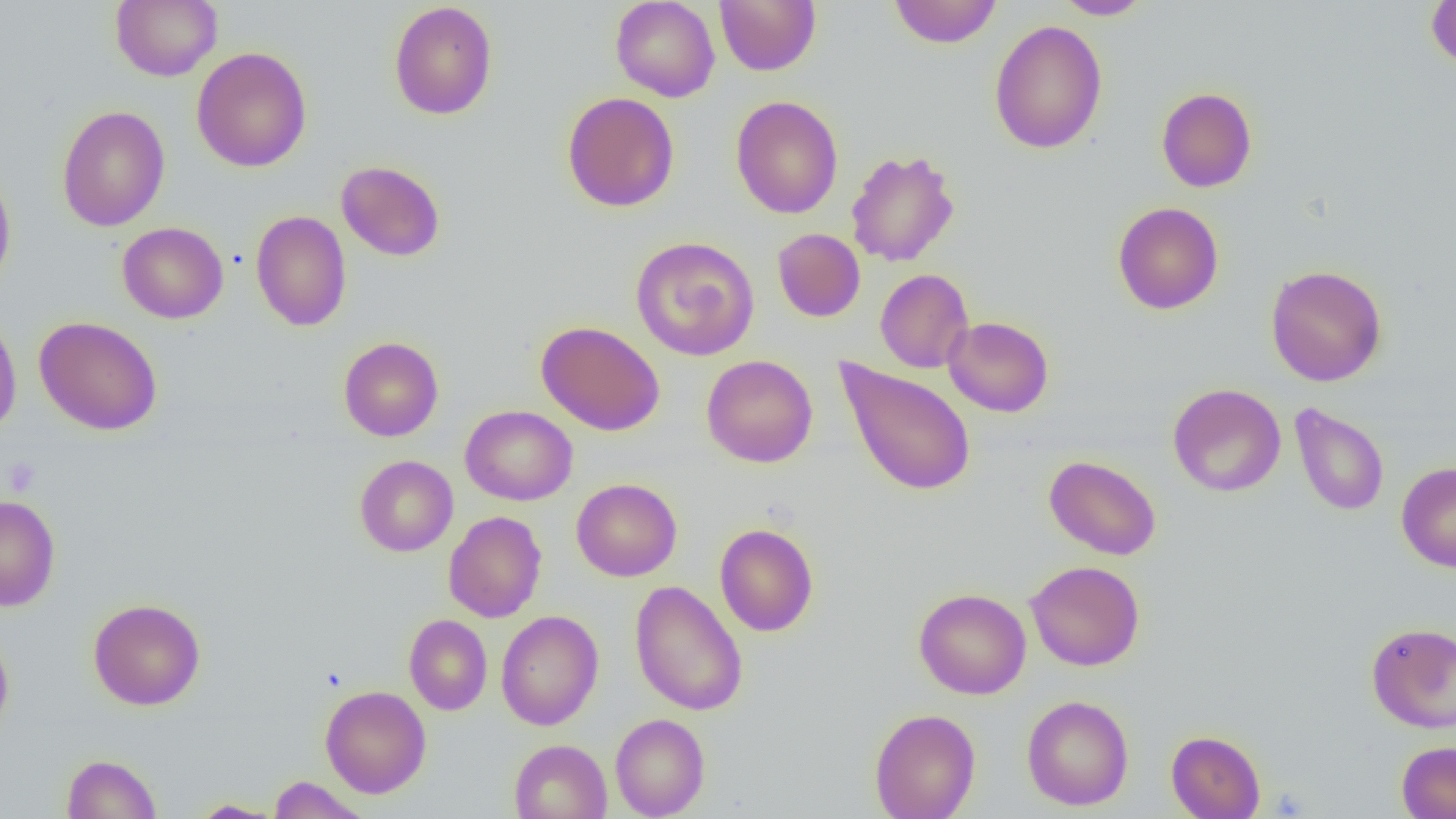

Approximate bounding boxes as [x1, y1, x2, y2] in pixels. Uninfected red blood cell locations: [111, 0, 222, 81], [610, 0, 721, 102], [714, 0, 821, 76], [888, 0, 1002, 49], [1053, 0, 1154, 19], [1426, 0, 1456, 71], [388, 2, 498, 120], [989, 19, 1107, 154], [192, 47, 312, 172], [1156, 87, 1257, 192], [562, 92, 680, 213], [730, 95, 843, 219], [56, 105, 171, 231], [846, 149, 960, 267], [336, 160, 445, 262], [0, 165, 16, 294], [1113, 202, 1224, 315], [250, 210, 351, 331], [117, 222, 228, 323], [772, 228, 865, 322], [630, 236, 759, 361], [1265, 264, 1387, 386], [875, 269, 974, 373], [0, 312, 22, 438], [33, 316, 163, 435], [944, 316, 1054, 417], [536, 321, 665, 436], [339, 336, 443, 441], [701, 354, 818, 468], [835, 358, 978, 498], [1168, 383, 1286, 497], [1289, 403, 1389, 516], [460, 405, 577, 506], [1044, 454, 1162, 560], [355, 455, 458, 556], [1396, 462, 1456, 572], [571, 478, 682, 581], [0, 496, 60, 611], [444, 511, 546, 623], [714, 523, 819, 637], [1025, 560, 1145, 671], [630, 580, 747, 716], [914, 588, 1031, 699], [88, 598, 206, 710], [495, 610, 603, 730], [404, 614, 492, 715], [1366, 622, 1456, 733], [0, 629, 14, 739], [320, 685, 431, 798], [1021, 694, 1134, 811], [869, 708, 980, 819], [610, 713, 710, 818], [1166, 730, 1266, 819], [509, 739, 612, 819], [1397, 741, 1456, 818], [61, 753, 162, 818], [268, 776, 369, 819], [187, 799, 286, 818]. Platelet locations: [2, 457, 41, 497]. Slide-level diagnosis: negative for blood parasites. Thin blood film. 1000x magnification. Single field of view. Image is 1456×819 pixels. Light microscopy.